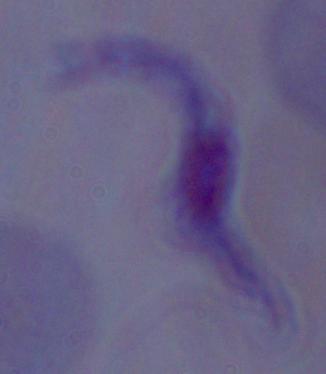
Photomicrograph. A trypanosome is seen. 1000x magnification.